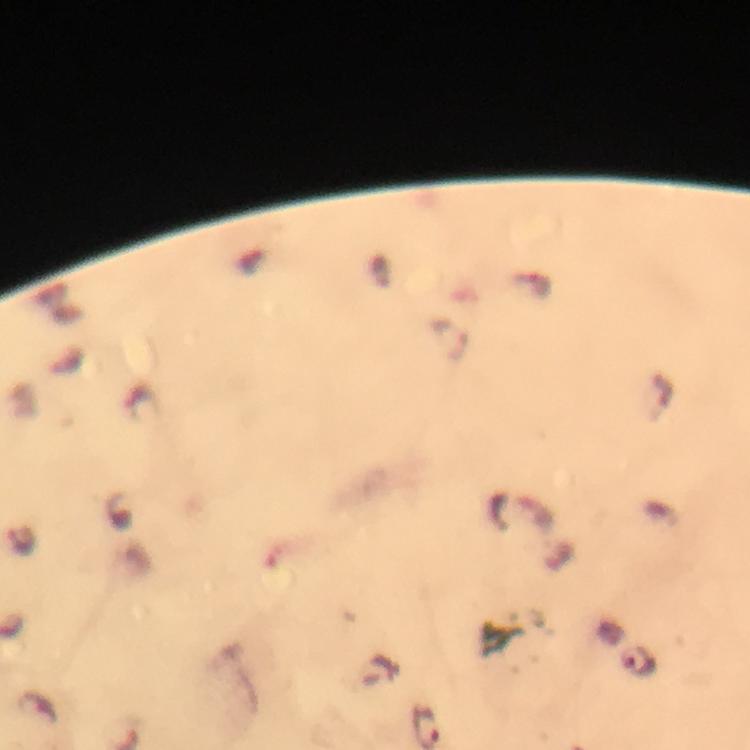 Approximate centers as (x, y) in pixels. Malaria parasite locations: (530, 285), (452, 338), (21, 540), (637, 661). Giemsa-stained preparation. Smartphone photograph taken through a microscope. 100x magnification. Thick blood smear. Immersion oil was used. Image is 750×750 pixels. From a malaria diagnostic workup. A crop from one field of view.